Give the position of every malaria parasite.
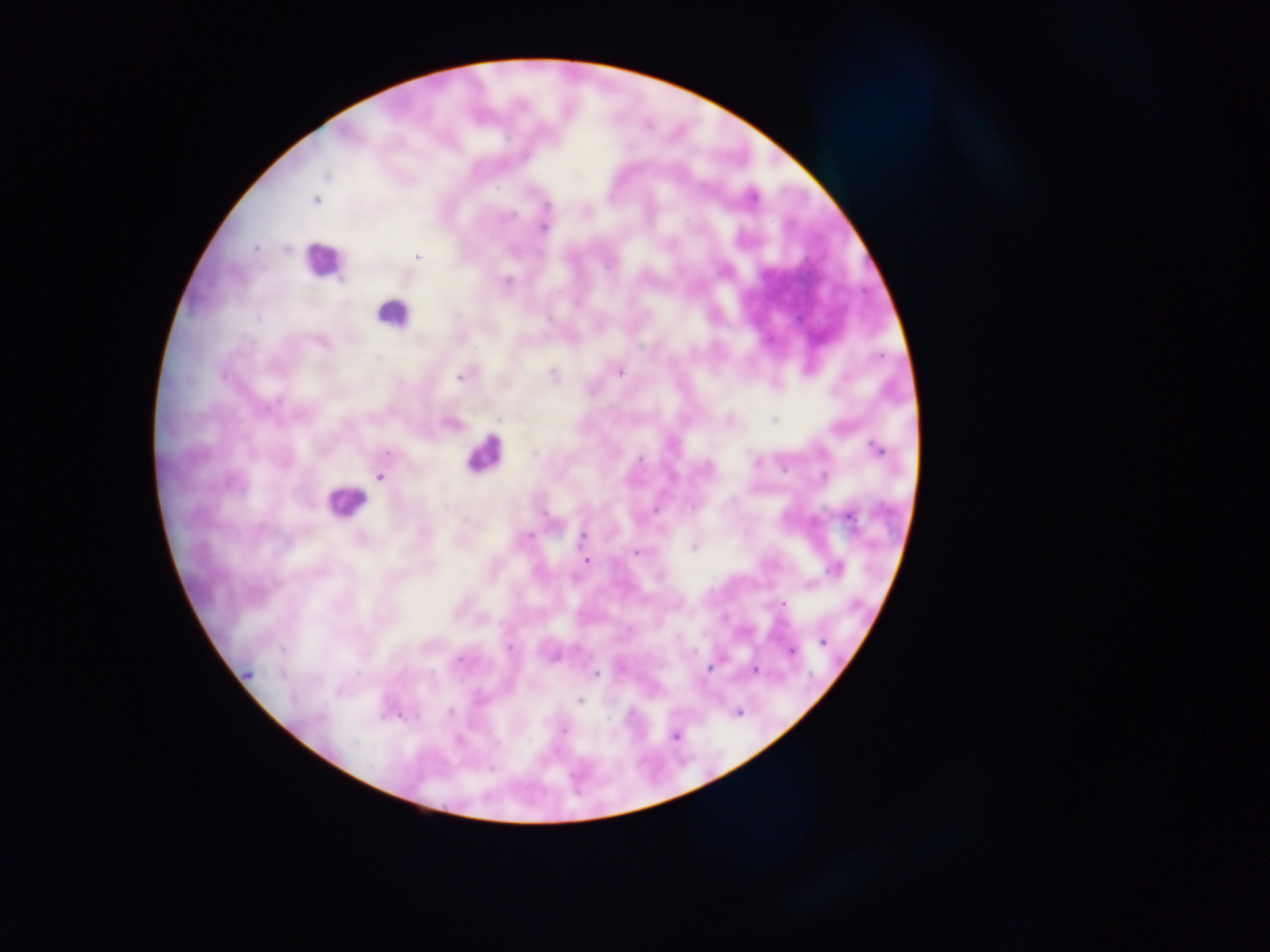
Approximate centers as [x, y] in pixels.
Malaria parasites: [315, 199], [543, 226], [255, 247], [418, 256], [506, 281], [321, 340], [620, 371], [462, 375], [553, 375], [450, 422], [877, 449], [380, 477], [847, 516], [583, 536], [694, 546], [637, 552], [586, 560], [834, 568], [782, 604], [822, 641], [791, 651], [711, 667], [621, 668], [756, 670], [595, 674], [580, 700], [563, 730], [675, 735].

preparation = thick blood smear
capture = mobile-phone photograph through a microscope
image size = 1270×952 pixels
country = Ghana
leukocyte locations = approximate centers as [x, y] in pixels: [322, 261], [392, 313], [484, 453], [346, 502]
field of view = single